Identify the preparation type.
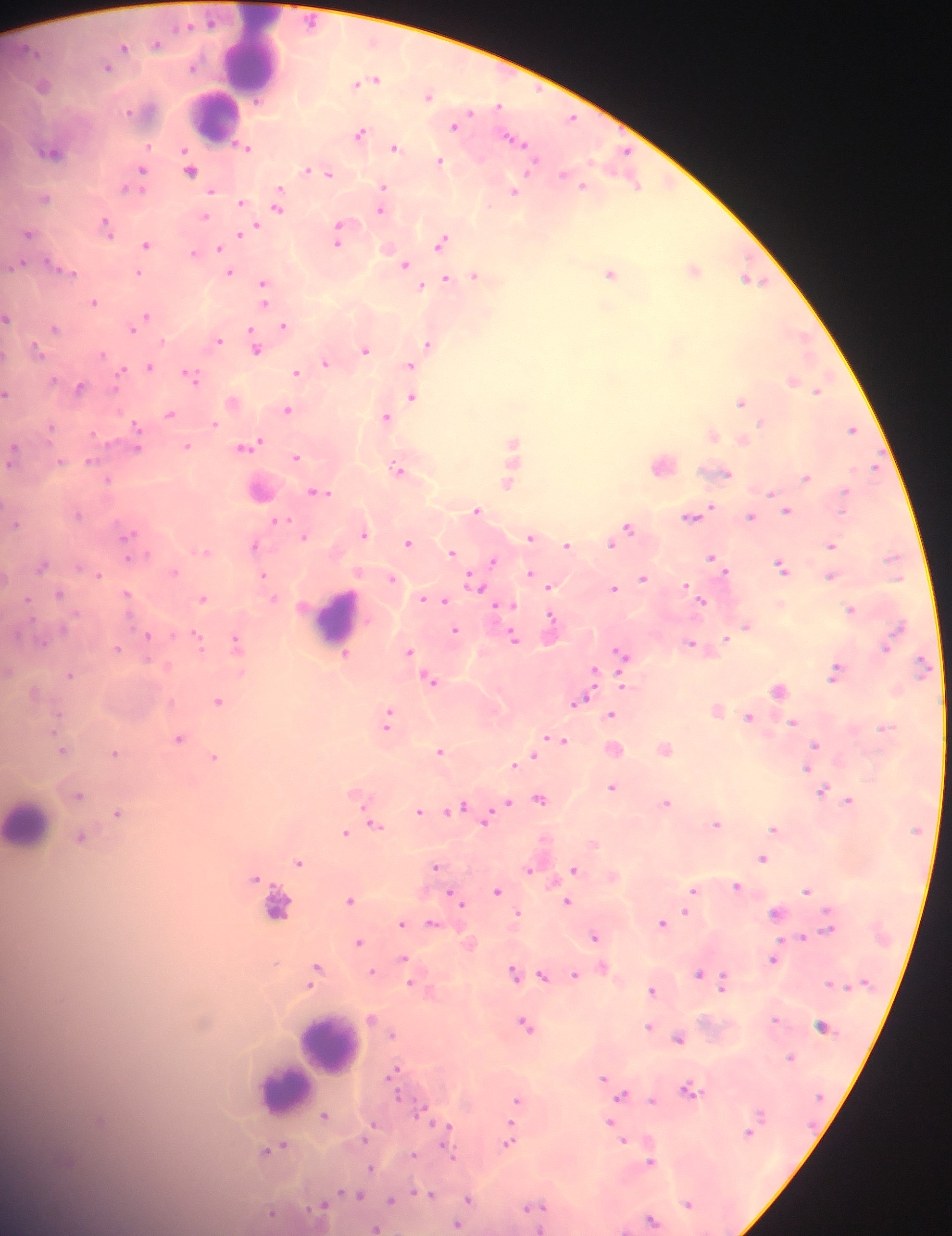
Thick blood smear.

{
  "field_of_view": "single",
  "leukocyte_locations": "approximate centers as x y in pixels: 250 54; 214 115; 337 616; 28 823; 278 912; 327 1044; 283 1088",
  "country": "Ghana",
  "image_size": "952×1236 pixels",
  "capture": "mobile-phone photograph through a microscope",
  "malaria_parasite_locations": "approximate centers as x y in pixels: 156 44; 123 47; 106 66; 370 80; 42 85; 428 95; 456 124; 359 132; 513 139; 244 147; 394 147; 53 151; 439 160; 190 168; 312 169; 141 171; 325 172; 137 177; 634 182; 581 184; 383 190; 513 191; 44 198; 240 202; 276 205; 381 208; 204 217; 105 224; 248 230; 339 230; 28 233; 241 233; 442 241; 146 244; 218 248; 193 253; 20 264; 404 264; 61 269; 693 269; 230 272; 140 273; 611 273; 474 275; 750 279; 445 280; 262 286; 420 286; 264 294; 93 302; 7 317; 144 318; 284 325; 132 326; 54 328; 218 340; 428 343; 255 347; 365 349; 36 350; 325 362; 409 365; 149 367; 296 372; 190 376; 792 381; 80 386; 819 389; 7 393; 411 396; 233 401; 740 401; 288 409; 168 414; 385 416; 213 422; 852 428; 136 429; 711 433; 742 439; 512 444; 187 446; 248 446; 12 453; 295 456; 89 461; 663 463; 509 465; 398 469; 720 472; 806 477; 108 479; 508 482; 260 489; 317 492; 476 510; 786 510; 77 513; 692 516; 751 516; 281 520; 14 522; 627 526; 364 532; 127 535; 304 536; 531 537; 408 542; 612 543; 255 545; 568 545; 830 545; 203 551; 451 551; 493 560; 716 562; 43 564; 782 566; 531 574; 830 575; 263 576; 643 578; 392 579; 538 579; 475 584; 549 585; 613 588; 60 594; 127 595; 203 598; 424 598; 273 599; 444 600; 701 600; 502 604; 851 609; 551 623; 746 625; 455 630; 147 635; 512 636; 197 638; 237 641; 692 644; 116 648; 409 653; 621 653; 344 655; 836 671; 593 672; 70 675; 431 679; 780 689; 579 700; 218 701; 717 709; 611 714; 750 716; 389 718; 793 722; 179 738; 554 739; 815 745; 614 748; 664 748; 62 749; 440 751; 115 753; 532 755; 214 757; 516 764; 807 768; 612 787; 822 791; 358 793; 78 795; 539 798; 849 800; 666 802; 506 803; 458 808; 420 810; 494 811; 119 813; 486 817; 375 824; 716 824; 774 828; 355 829; 345 832; 80 838; 763 858; 298 861; 436 866; 530 869; 573 869; 256 877; 737 887; 497 889; 693 889; 807 890; 455 896; 350 899; 567 901; 685 912; 776 912; 518 913; 401 922; 662 922; 433 923; 595 937; 803 937; 359 941; 404 958; 774 958; 602 967; 316 970; 514 971; 373 972; 698 974; 543 975; 575 975; 722 980; 412 983; 652 990; 371 1018; 774 1019; 525 1026; 821 1026; 648 1027; 392 1034; 678 1038; 790 1056; 394 1073; 604 1077; 606 1082; 688 1090; 622 1095; 653 1100; 517 1101; 425 1110; 324 1115; 609 1121; 372 1125; 445 1128; 748 1131; 509 1139; 624 1141; 276 1148; 412 1155; 651 1161; 371 1167; 430 1194; 356 1195; 469 1199; 391 1200; 688 1203; 323 1205; 532 1207; 272 1213; 652 1219; 457 1225; 375 1228"
}